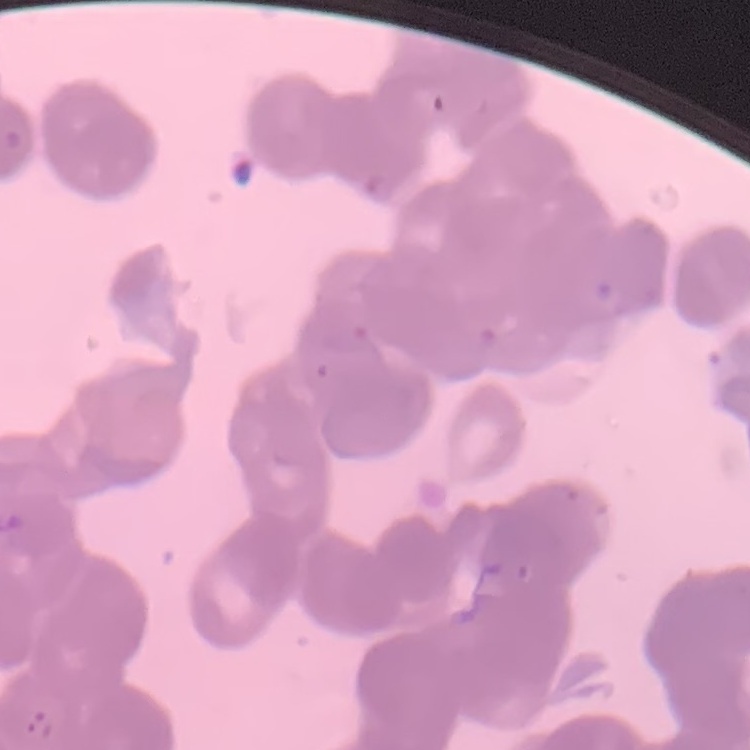

red blood cell morphology = rouleaux formation
preparation = thin peripheral smear
image type = square crop of a larger photomicrograph
stain = Field's or Giemsa